Locate every uninfected red blood cell.
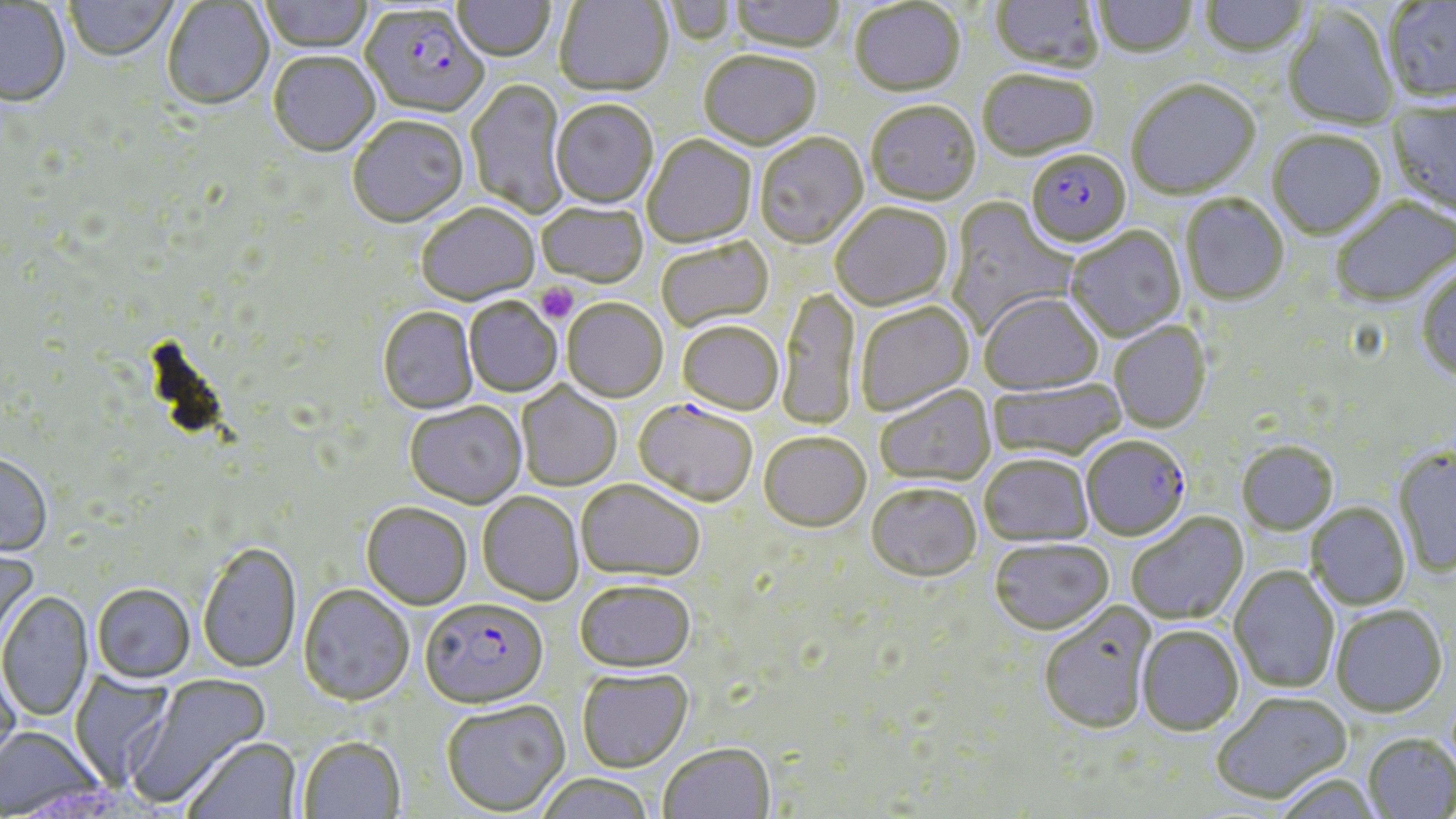

Approximate bounding boxes as (x1,y1)-(x2,y2) corner pairs in pixels.
Uninfected red blood cells: (260,0)-(374,55), (454,0)-(555,63), (554,0)-(673,99), (662,0)-(736,47), (731,0)-(845,55), (990,0)-(1103,76), (1199,0)-(1310,59), (64,1)-(178,63), (850,1)-(966,100), (1093,1)-(1196,60), (1383,1)-(1456,105), (162,2)-(274,112), (0,3)-(71,110), (1283,9)-(1399,132), (699,53)-(822,152), (268,54)-(380,159), (978,72)-(1099,163), (465,79)-(569,218), (1127,82)-(1262,201), (551,101)-(658,210), (1387,102)-(1456,219), (866,104)-(981,207), (347,118)-(470,229), (1267,132)-(1386,242), (755,134)-(868,250), (642,136)-(757,250), (1181,195)-(1290,307), (946,198)-(1077,338), (1331,198)-(1455,308), (537,203)-(648,290), (830,204)-(952,313), (416,206)-(541,308), (1066,228)-(1186,343), (657,239)-(774,332), (1416,268)-(1456,384), (779,287)-(859,431), (979,294)-(1104,396), (464,299)-(562,398), (562,300)-(668,403), (855,303)-(975,416), (377,308)-(478,415), (677,322)-(784,415), (1109,322)-(1211,434), (988,378)-(1126,463), (516,383)-(622,491), (875,385)-(997,488), (404,403)-(527,510), (759,433)-(871,533), (1236,442)-(1338,536), (1393,449)-(1456,577), (978,455)-(1094,547), (0,456)-(53,559), (576,480)-(705,583), (866,484)-(982,583), (478,493)-(584,606), (1306,503)-(1410,609), (361,504)-(472,612), (1126,513)-(1249,625), (989,539)-(1113,636), (198,543)-(302,675), (0,544)-(40,657), (1229,567)-(1339,693), (574,582)-(696,675), (92,586)-(195,685), (298,587)-(414,708), (0,592)-(94,724), (1038,602)-(1157,736), (1331,606)-(1448,718), (1137,626)-(1244,736), (0,658)-(21,780), (70,670)-(175,789), (577,671)-(693,773), (128,675)-(272,808), (1212,691)-(1352,804), (441,701)-(570,817), (0,727)-(108,818), (1363,734)-(1455,818), (183,738)-(302,819), (298,738)-(405,819), (659,744)-(775,819), (1273,773)-(1383,818), (535,775)-(655,819).

Plasmodium falciparum-infected red blood cell locations: (360,8)-(488,120), (1026,152)-(1131,251), (633,399)-(759,507), (1081,437)-(1190,542), (420,601)-(548,711). Platelet locations: (535,283)-(578,323). Slide-level diagnosis: Plasmodium falciparum. Image is 1456×819 pixels. May-Grünwald-Giemsa stain. Thin blood film. Single field of view. 1000x magnification. Light microscopy.